State the blood parasite species.
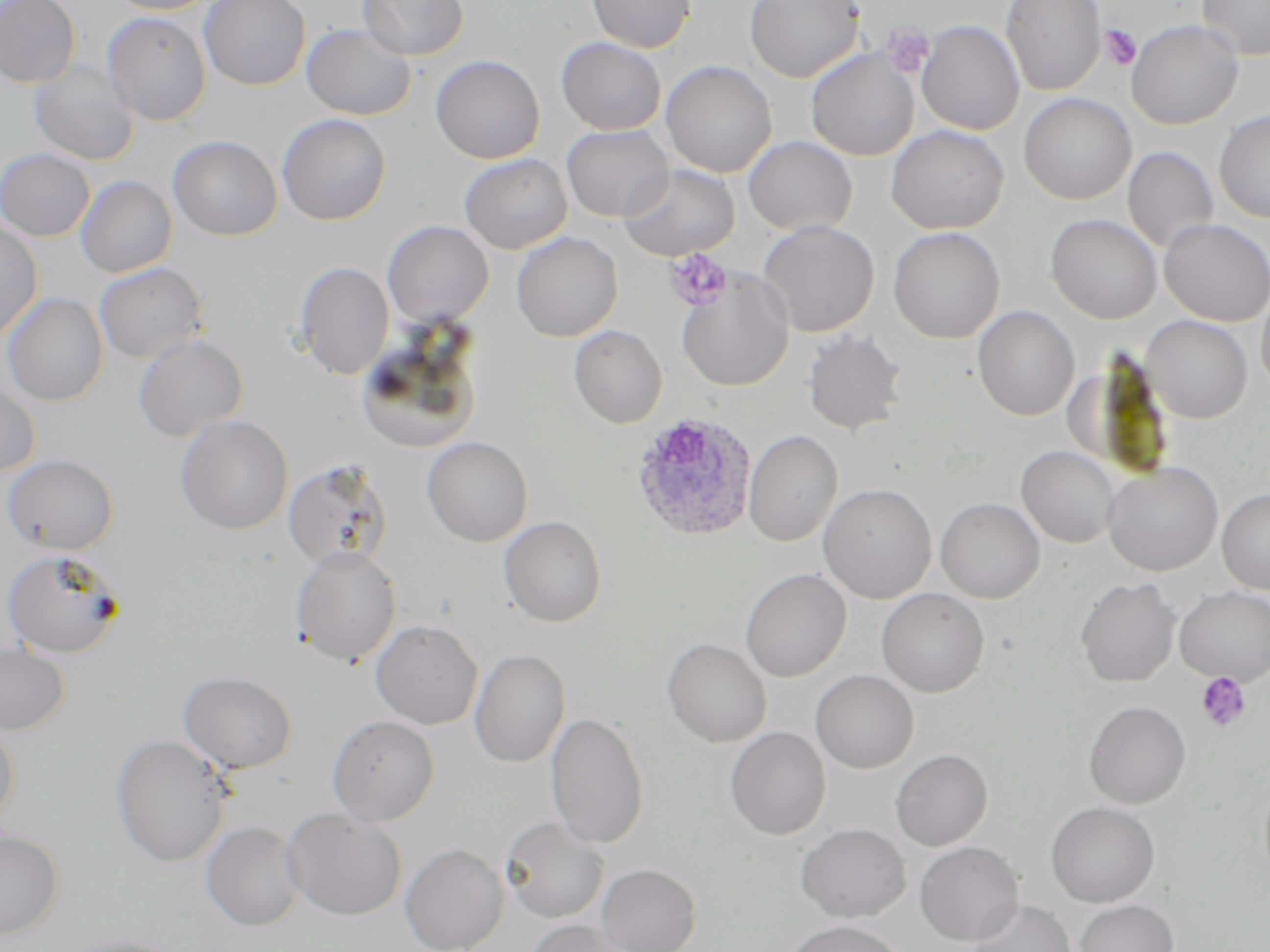

Plasmodium ovale.

Summary:
  - Coordinate format: approximate bounding boxes as [x1, y1, x2, y2] in pixels
  - Platelet locations: [882, 23, 935, 79], [1099, 24, 1142, 71], [664, 249, 732, 311], [1196, 672, 1252, 733]
  - Uninfected red blood cell locations: [0, 0, 81, 89], [108, 0, 221, 15], [199, 0, 311, 91], [359, 0, 468, 60], [586, 0, 696, 53], [744, 0, 864, 83], [1000, 0, 1106, 96], [1197, 0, 1270, 60], [102, 11, 211, 126], [1126, 19, 1243, 130], [916, 20, 1025, 135], [301, 23, 416, 120], [556, 37, 667, 135], [806, 49, 919, 161], [430, 54, 545, 164], [29, 60, 139, 166], [660, 60, 777, 178], [1018, 93, 1137, 205], [1215, 110, 1270, 224], [277, 114, 391, 226], [561, 125, 673, 222], [886, 125, 1009, 234], [167, 135, 281, 241], [743, 135, 857, 236], [1123, 147, 1219, 253], [0, 148, 95, 241], [459, 153, 572, 254], [619, 164, 740, 261], [75, 176, 177, 277], [1045, 213, 1162, 324], [0, 217, 44, 342], [1159, 219, 1270, 326], [382, 220, 494, 328], [757, 220, 879, 337], [888, 227, 1005, 343], [511, 231, 623, 342], [293, 261, 394, 380], [94, 262, 209, 364], [676, 269, 794, 392], [1256, 282, 1270, 397], [2, 292, 108, 406], [973, 305, 1080, 421], [1141, 315, 1253, 423], [568, 324, 668, 428], [801, 329, 907, 436], [354, 332, 482, 454], [133, 334, 248, 441], [0, 378, 41, 476], [175, 415, 293, 534], [743, 430, 843, 547], [421, 436, 533, 546], [1016, 445, 1122, 547], [2, 453, 120, 555], [283, 459, 393, 572], [1102, 462, 1223, 576], [817, 483, 937, 604], [1217, 488, 1270, 595], [935, 497, 1045, 603], [498, 515, 607, 627], [290, 545, 401, 667], [2, 549, 124, 658], [740, 568, 851, 682], [1074, 577, 1182, 688], [1174, 586, 1270, 686], [876, 587, 990, 697], [370, 620, 483, 729], [662, 638, 772, 747], [0, 643, 70, 735], [469, 649, 570, 768], [178, 670, 297, 774], [810, 670, 919, 774], [1084, 700, 1191, 808], [545, 712, 649, 849], [0, 714, 21, 828], [326, 715, 440, 825], [724, 727, 831, 840], [109, 734, 233, 867], [891, 749, 992, 851], [1046, 801, 1160, 908], [283, 808, 407, 921], [500, 817, 609, 923], [201, 821, 305, 932], [795, 823, 910, 922], [0, 827, 64, 941], [914, 841, 1024, 946], [400, 842, 508, 952], [596, 863, 701, 952], [966, 899, 1076, 952], [1073, 899, 1178, 952], [525, 919, 633, 952], [782, 919, 908, 952], [60, 935, 187, 952]
  - Plasmodium ovale-infected red blood cell locations: [630, 412, 758, 542]
  - Field of view: one of a larger specimen
  - Modality: optical microscopy
  - Preparation: thin blood smear
  - Image size: 1270×952 pixels
  - Magnification: 1000x
  - Stain: May-Grünwald-Giemsa